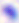
Toxoplasma gondii is seen. 400x magnification. Micrograph.